State which parasite is depicted.
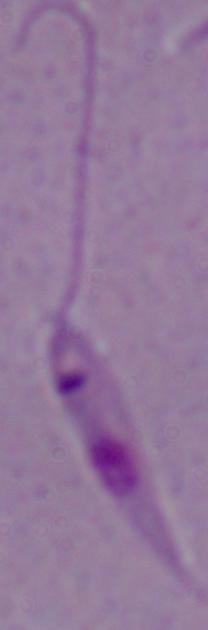

Leishmania.

modality = micrograph
magnification = 1000x